Report the malaria status of this cell.
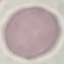
Uninfected.

Thin blood smear. Giemsa-stained preparation. Acquired by smartphone through the microscope eyepiece. Automatically extracted cell patch, resized to 64 × 64 pixels.